Evaluate for malaria.
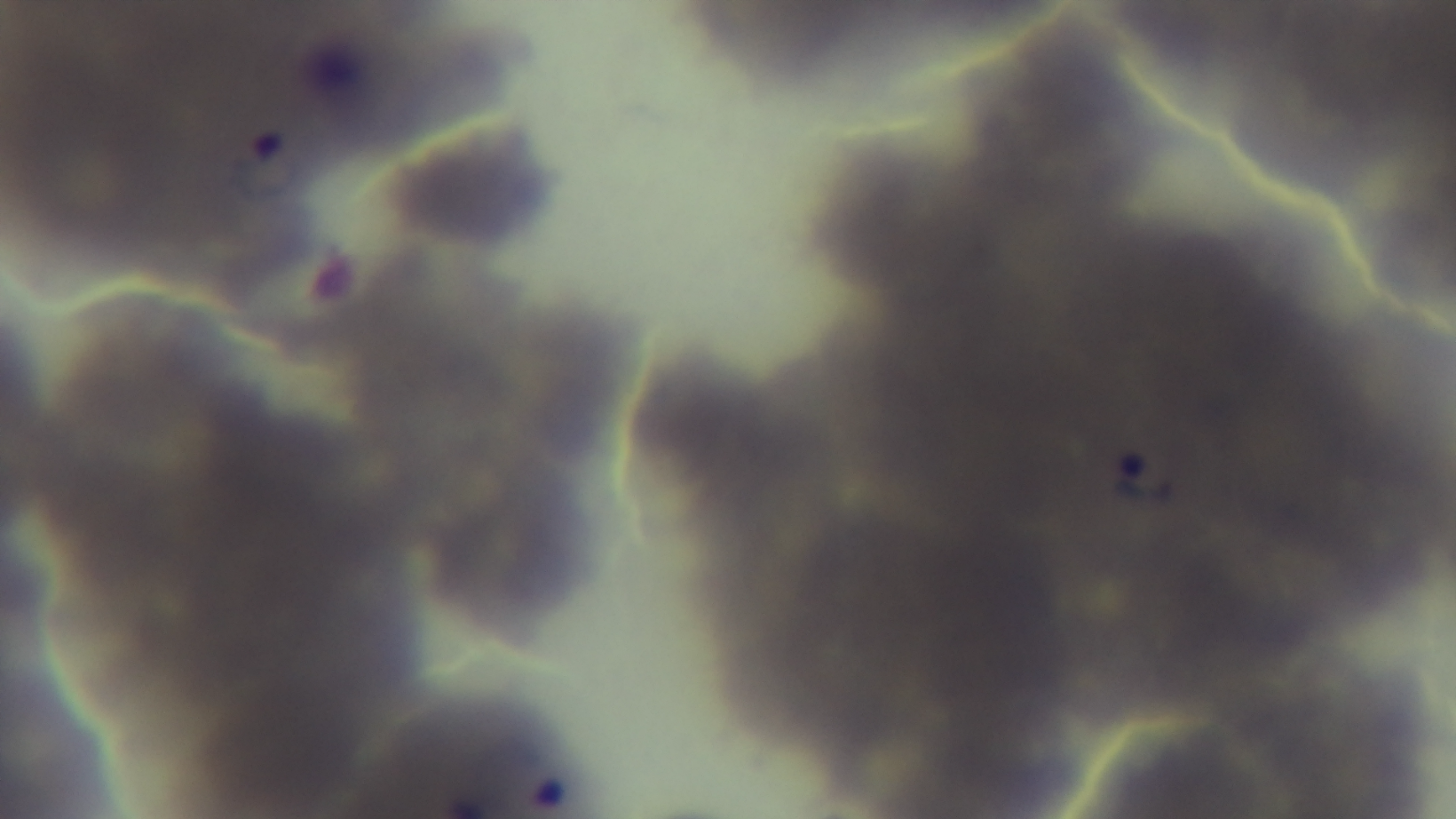
Positive.

Single field of view. Oil-immersion objective, 100x. Giemsa-stained. Preparation: thin smear. Mounted 4K digital camera. Photomicrograph.